Comment on the morphology of the red blood cells.
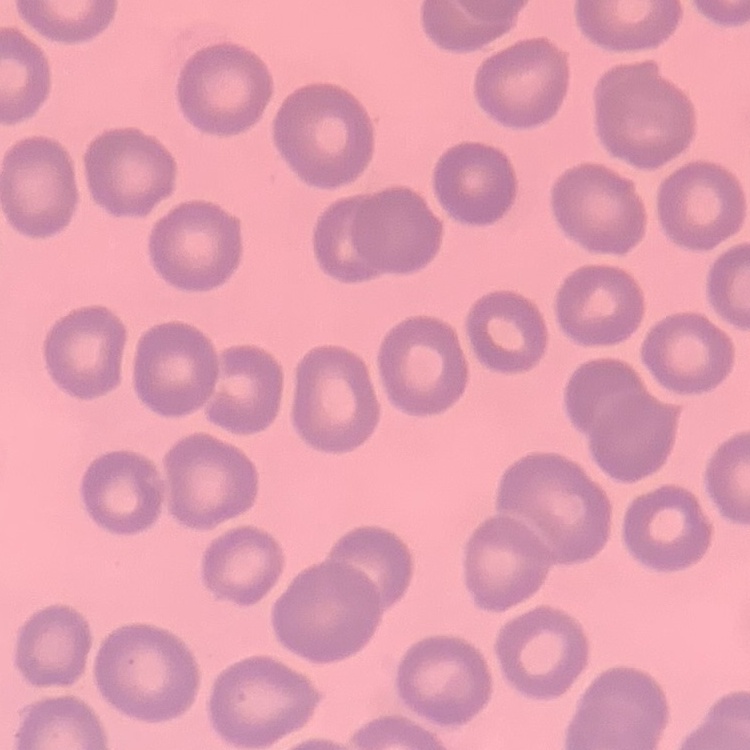

No rouleaux formation.

preparation = thin blood film
stain = Field's or Giemsa
image type = one tile cut from a larger photomicrograph